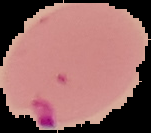

{
  "preparation": "thin blood smear",
  "malaria_status": "parasitized",
  "image_size": "151×133 pixels",
  "image_type": "cell region segmented out of the field of view; surrounding area masked to black"
}